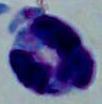
magnification = 1000x
modality = micrograph
identification = white blood cell